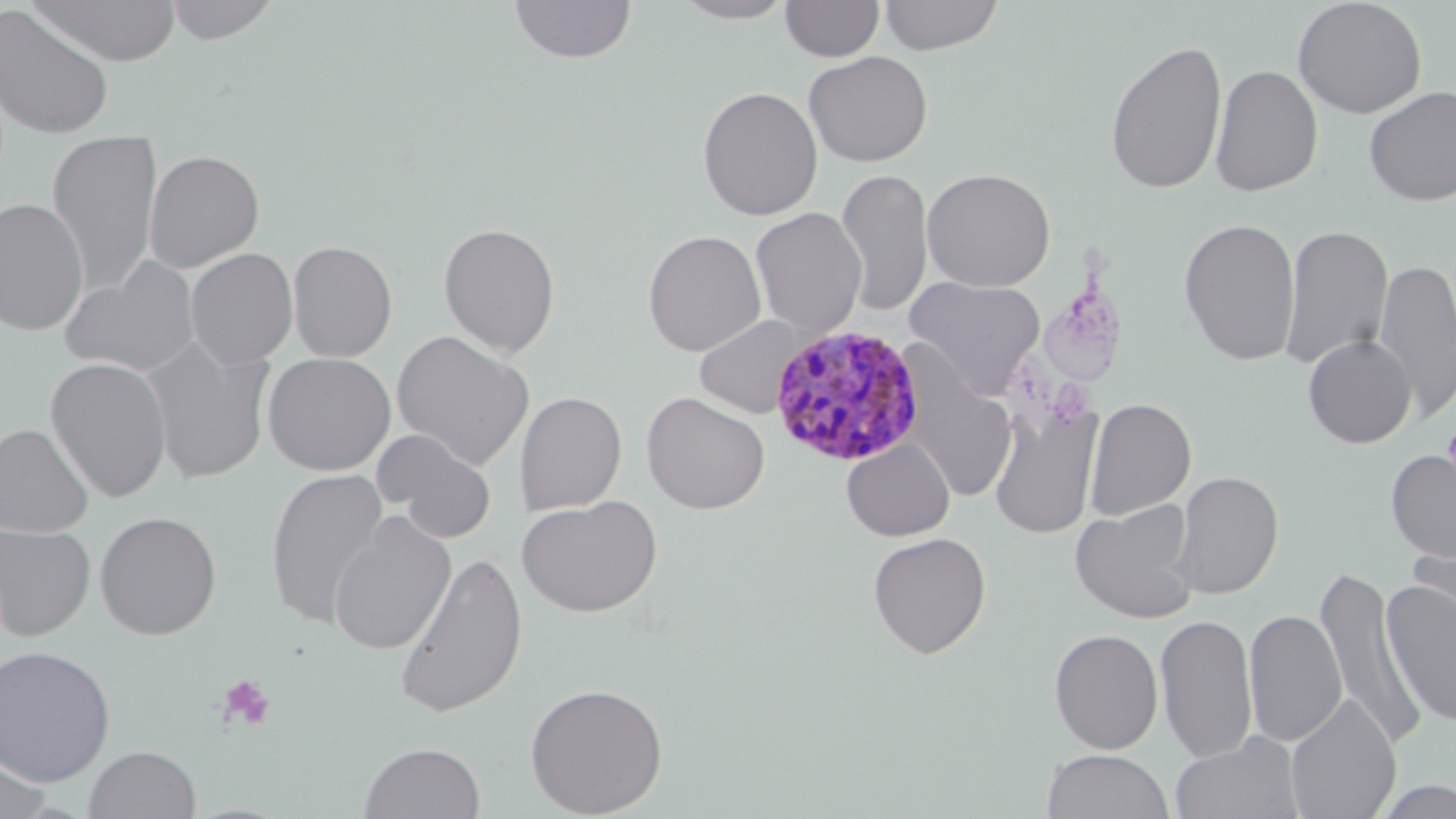
Summary:
  - Coordinate format: approximate bounding boxes as (x1,y1)-(x2,y2) corner pairs in pixels
  - Platelet locations: (1442,412)-(1456,495), (215,673)-(277,732)
  - Uninfected red blood cell locations: (162,0)-(283,45), (508,0)-(637,64), (672,0)-(796,23), (780,0)-(885,62), (877,0)-(1005,55), (1292,0)-(1427,119), (28,1)-(181,66), (0,5)-(115,140), (1104,38)-(1227,195), (803,51)-(933,167), (1210,64)-(1323,197), (697,86)-(823,221), (1363,86)-(1456,206), (46,130)-(161,295), (144,150)-(265,272), (834,168)-(934,317), (921,168)-(1056,292), (0,197)-(89,336), (750,207)-(867,340), (1179,217)-(1301,366), (438,221)-(561,357), (1280,223)-(1394,370), (642,229)-(766,357), (287,240)-(398,362), (186,247)-(298,368), (59,255)-(201,378), (1374,258)-(1456,421), (905,275)-(1046,401), (694,314)-(805,418), (391,330)-(535,470), (1303,334)-(1416,448), (140,338)-(274,485), (262,352)-(396,475), (44,357)-(172,503), (901,373)-(1018,503), (515,391)-(627,515), (641,392)-(770,514), (1085,398)-(1196,520), (989,402)-(1102,539), (0,423)-(94,538), (372,428)-(498,542), (842,438)-(954,541), (1385,447)-(1456,567), (264,467)-(390,628), (1170,470)-(1285,599), (518,495)-(662,617), (1070,499)-(1200,624), (94,510)-(222,640), (328,513)-(457,656), (0,522)-(96,641), (1407,528)-(1456,643), (867,532)-(991,659), (393,552)-(529,719), (1314,564)-(1424,750), (1381,577)-(1456,730), (1243,609)-(1347,748), (1155,613)-(1258,763), (1049,629)-(1164,753), (0,644)-(116,786), (525,682)-(668,817), (1286,696)-(1401,819), (1170,734)-(1304,819), (358,741)-(485,819), (0,744)-(53,819), (84,745)-(202,819), (1042,749)-(1173,819), (1369,777)-(1456,818)
  - Plasmodium malariae-infected red blood cell locations: (770,323)-(927,470)
  - Slide-level diagnosis: Plasmodium malariae
  - Field of view: one of a larger specimen
  - Image size: 1456×819 pixels
  - Preparation: thin blood smear
  - Modality: optical microscopy
  - Magnification: 1000x
  - Stain: May-Grünwald-Giemsa